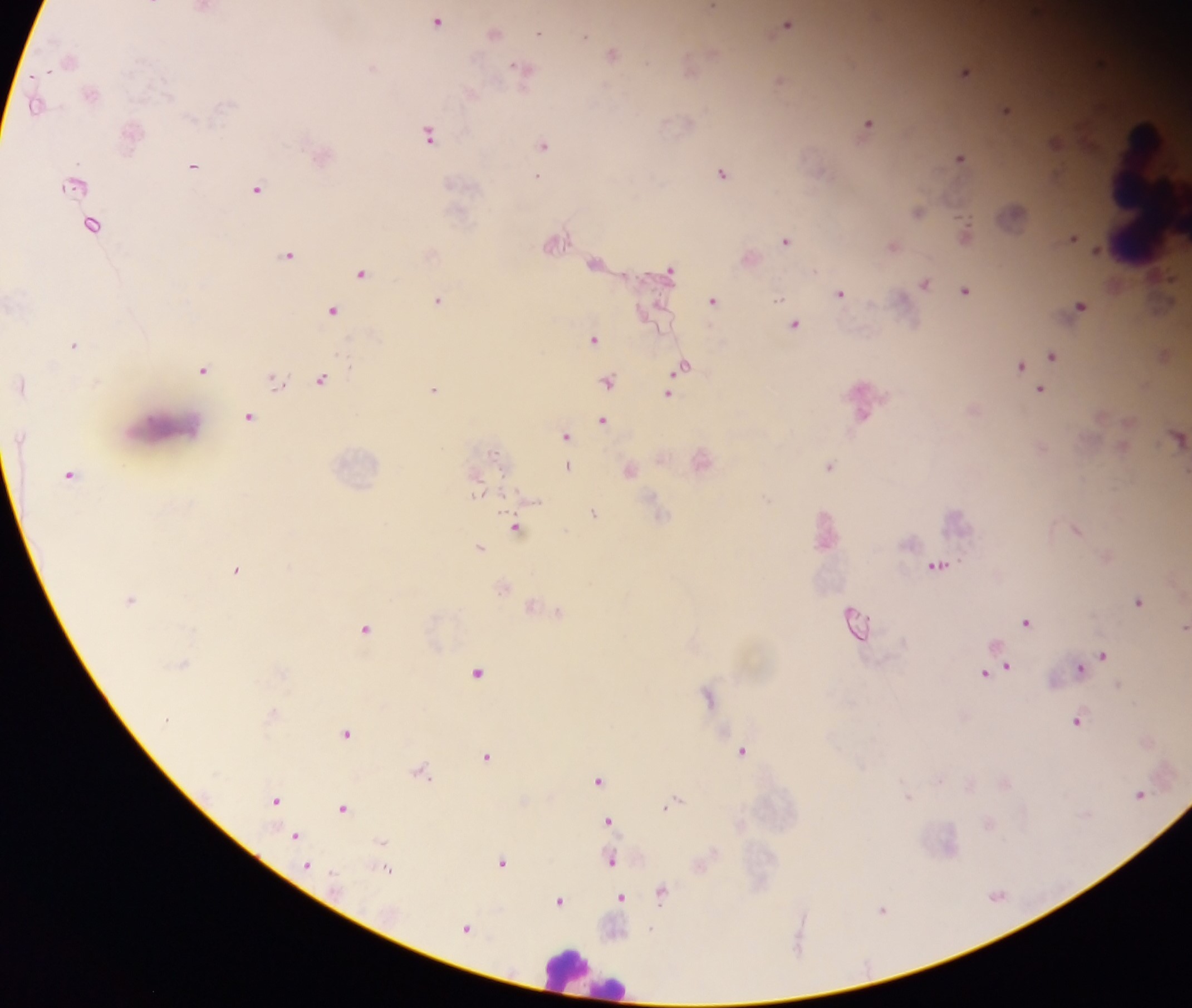
Approximate centers as {x, y} in pixels.
Summary:
  - Plasmodium parasite locations: {713, 6}, {437, 21}, {788, 23}, {495, 32}, {538, 33}, {585, 35}, {613, 53}, {1102, 61}, {517, 65}, {965, 70}, {779, 79}, {1005, 108}, {868, 123}, {430, 133}, {1055, 141}, {543, 144}, {960, 157}, {193, 165}, {722, 173}, {538, 176}, {257, 188}, {917, 210}, {965, 230}, {1073, 237}, {786, 240}, {893, 245}, {289, 253}, {595, 262}, {670, 269}, {362, 272}, {925, 282}, {965, 291}, {841, 293}, {438, 298}, {713, 300}, {1080, 305}, {333, 310}, {794, 324}, {595, 338}, {74, 344}, {1052, 354}, {1019, 365}, {204, 369}, {678, 373}, {275, 379}, {321, 379}, {609, 381}, {670, 387}, {434, 388}, {1040, 389}, {861, 398}, {250, 416}, {604, 419}, {565, 435}, {495, 453}, {568, 465}, {830, 465}, {478, 483}, {594, 512}, {515, 527}, {1077, 529}, {480, 546}, {937, 564}, {237, 569}, {1139, 600}, {558, 610}, {854, 621}, {1026, 621}, {1185, 625}, {367, 628}, {1103, 654}, {1079, 667}, {1004, 668}, {477, 671}, {993, 671}, {708, 694}, {1078, 720}, {347, 733}, {743, 750}, {488, 755}, {421, 771}, {598, 779}, {1140, 793}, {275, 799}, {674, 801}, {343, 807}, {608, 821}, {296, 835}, {382, 841}, {611, 859}, {502, 861}, {308, 865}, {387, 869}, {662, 891}, {621, 898}, {559, 901}, {883, 909}, {467, 927}, {653, 928}
  - Leukocyte locations: {1147, 192}, {169, 430}, {583, 972}
  - Image size: 1192×1008 pixels
  - Country: Ghana
  - Field of view: single
  - Preparation: thick blood smear
  - Capture: mobile-phone photograph through a microscope